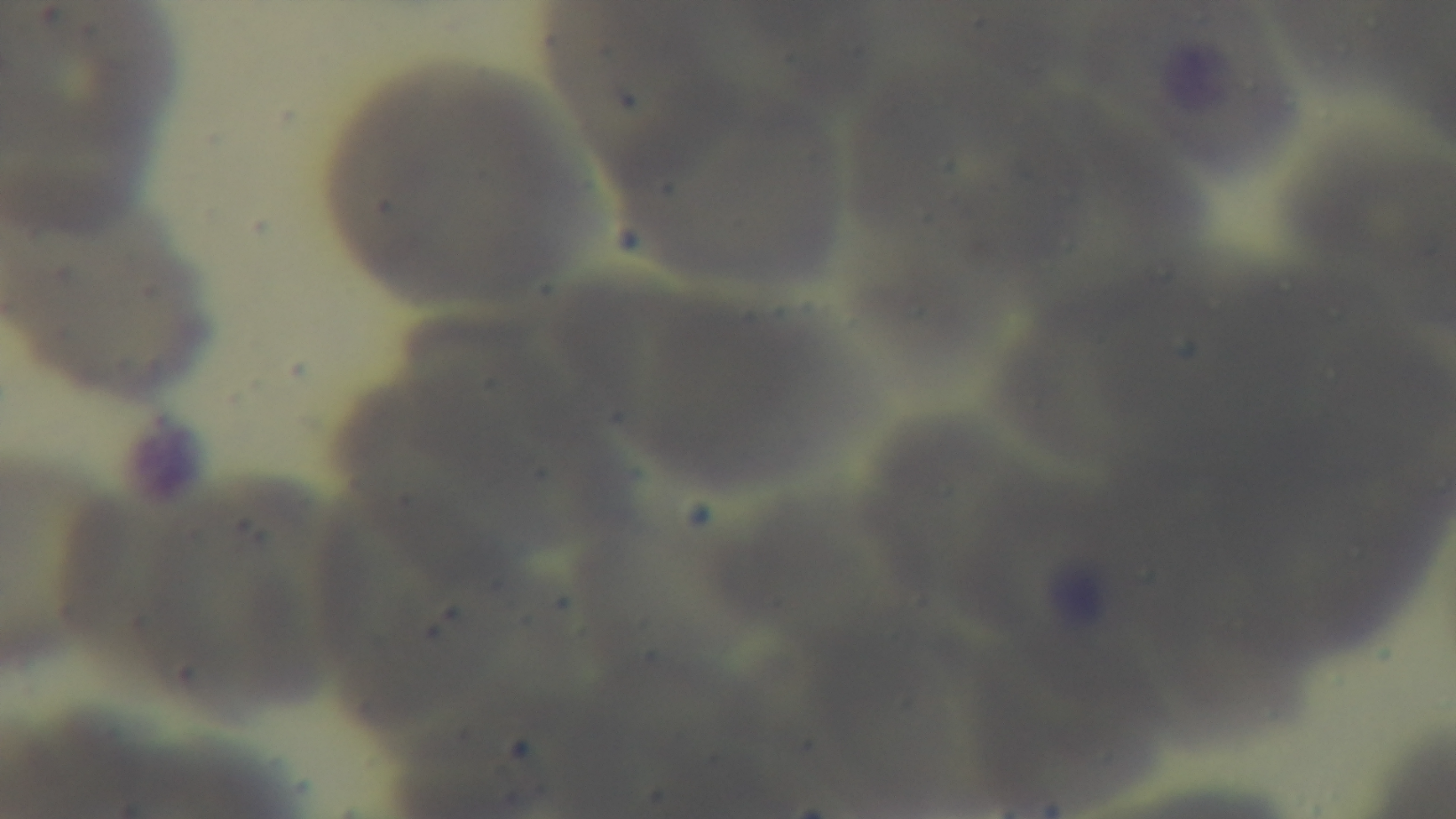
{
  "malaria_status": "negative",
  "objective": "100x oil immersion",
  "stain": "Giemsa",
  "preparation": "thin smear",
  "field_of_view": "single",
  "modality": "light microscopy",
  "capture": "mounted 4K digital camera"
}